Locate every blood parasite and identify its species.
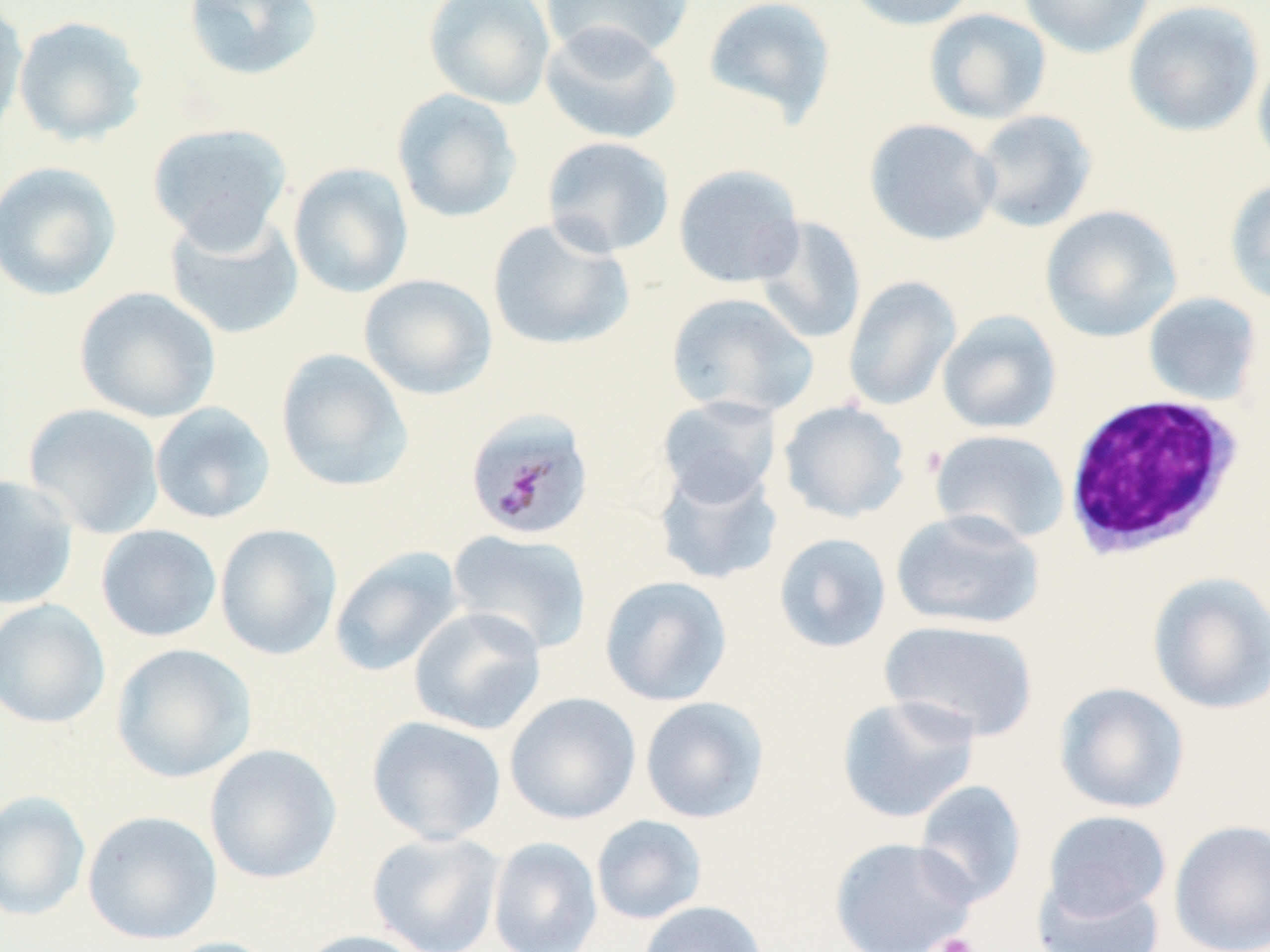
Approximate bounding boxes as [x1, y1, x2, y2] in pixels.
Plasmodium malariae-infected red blood cells: [464, 408, 595, 542].
No Plasmodium falciparum, Plasmodium ovale, Plasmodium vivax, Babesia divergens, or Trypanosoma brucei observed.

Summary:
  - White blood cell locations: [1061, 393, 1245, 560]
  - Platelet locations: [930, 932, 980, 952]
  - Uninfected red blood cell locations: [0, 0, 28, 145], [182, 0, 325, 82], [423, 0, 556, 109], [540, 0, 694, 64], [701, 0, 837, 128], [842, 0, 982, 31], [1018, 0, 1155, 59], [1124, 0, 1265, 137], [923, 8, 1052, 125], [12, 15, 149, 147], [540, 22, 681, 145], [1252, 50, 1270, 176], [391, 88, 522, 223], [970, 110, 1096, 233], [864, 118, 1001, 246], [147, 123, 293, 251], [541, 136, 675, 258], [0, 161, 121, 300], [288, 162, 414, 298], [673, 164, 805, 288], [1224, 178, 1270, 309], [1040, 205, 1182, 343], [164, 210, 304, 340], [754, 216, 866, 345], [487, 217, 635, 351], [358, 273, 498, 400], [843, 276, 961, 412], [74, 287, 221, 423], [665, 292, 818, 419], [1143, 292, 1262, 406], [937, 310, 1061, 435], [275, 349, 414, 492], [657, 394, 781, 507], [778, 399, 911, 523], [149, 402, 276, 525], [23, 403, 164, 539], [930, 429, 1070, 545], [653, 460, 784, 586], [0, 475, 79, 611], [890, 508, 1044, 630], [215, 523, 342, 660], [96, 524, 222, 642], [447, 529, 592, 655], [773, 532, 892, 654], [328, 546, 464, 677], [1147, 571, 1270, 714], [600, 575, 732, 706], [0, 599, 111, 729], [409, 605, 547, 734], [879, 618, 1039, 742], [111, 643, 256, 783], [1053, 681, 1190, 815], [504, 692, 641, 824], [835, 693, 982, 824], [640, 696, 769, 823], [367, 715, 507, 845], [204, 743, 342, 884], [913, 779, 1027, 907], [0, 790, 91, 921], [82, 810, 222, 944], [1042, 810, 1172, 920], [591, 815, 707, 925], [1168, 817, 1270, 952], [367, 831, 505, 952], [828, 835, 979, 952], [487, 836, 603, 952], [1032, 877, 1166, 952], [636, 900, 769, 952], [294, 930, 432, 952], [157, 936, 284, 952]
  - Slide-level diagnosis: Plasmodium malariae
  - Preparation: thin blood smear
  - Modality: light microscopy
  - Image size: 1270×952 pixels
  - Magnification: 1000x
  - Stain: May-Grünwald-Giemsa
  - Field of view: single